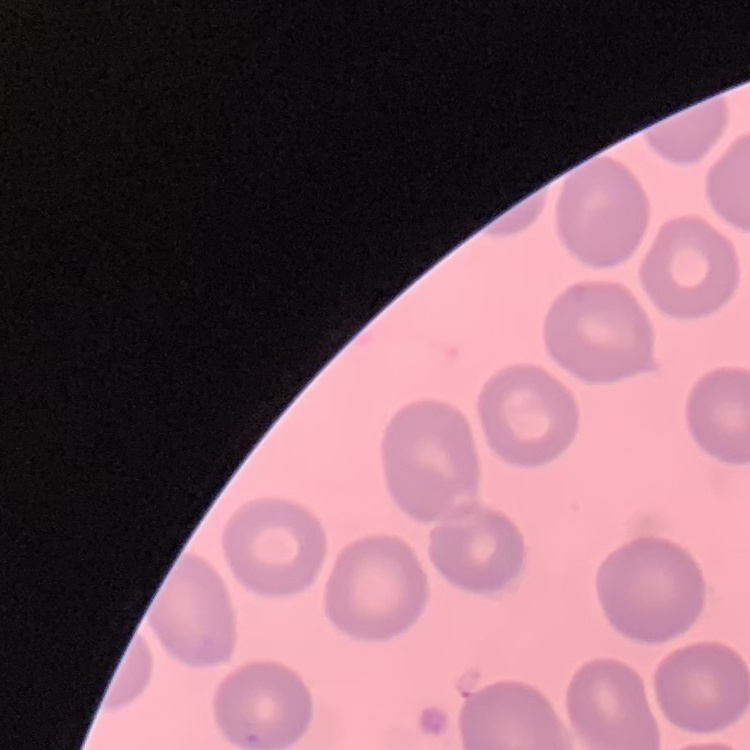

Summary:
  - Erythrocyte morphology: no rouleaux formation
  - Stain: Field's or Giemsa
  - Image type: square crop of a larger photomicrograph
  - Preparation: thin blood smear